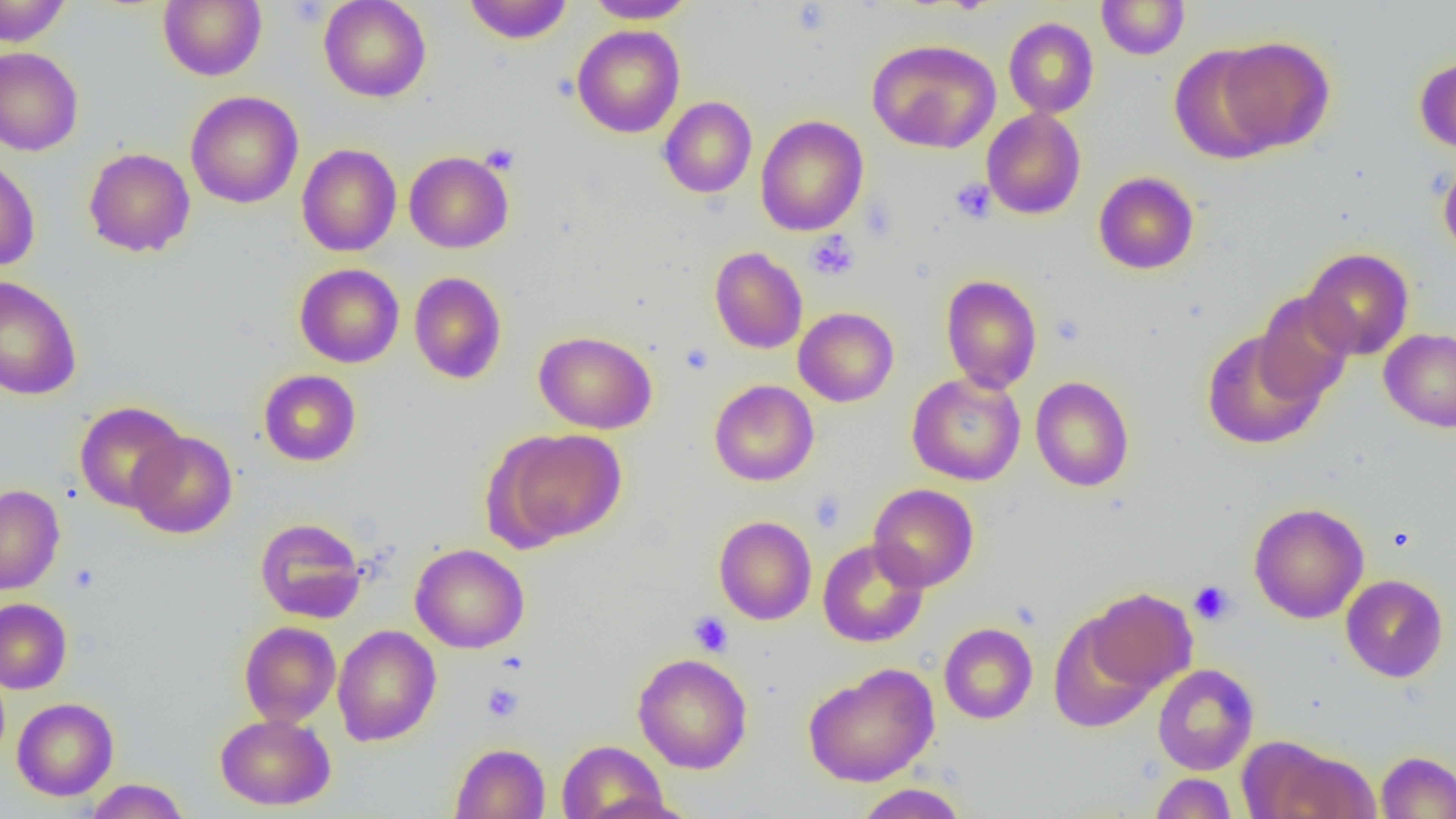

Summary:
  - Coordinate format: approximate bounding boxes as named x1/y1/x2/y2 corners in pixels
  - Uninfected red blood cell locations: (x1=0, y1=0, x2=71, y2=46), (x1=158, y1=0, x2=267, y2=81), (x1=318, y1=0, x2=432, y2=102), (x1=585, y1=0, x2=697, y2=24), (x1=1096, y1=0, x2=1189, y2=60), (x1=463, y1=1, x2=573, y2=44), (x1=1004, y1=17, x2=1099, y2=118), (x1=572, y1=25, x2=685, y2=138), (x1=1215, y1=36, x2=1335, y2=153), (x1=867, y1=38, x2=1001, y2=154), (x1=1169, y1=45, x2=1280, y2=164), (x1=0, y1=48, x2=83, y2=156), (x1=1415, y1=55, x2=1456, y2=154), (x1=186, y1=90, x2=303, y2=209), (x1=659, y1=96, x2=757, y2=198), (x1=981, y1=108, x2=1086, y2=219), (x1=755, y1=115, x2=868, y2=236), (x1=297, y1=143, x2=402, y2=256), (x1=84, y1=147, x2=195, y2=257), (x1=404, y1=151, x2=513, y2=253), (x1=0, y1=157, x2=40, y2=272), (x1=1438, y1=158, x2=1456, y2=262), (x1=1093, y1=171, x2=1199, y2=275), (x1=709, y1=247, x2=808, y2=354), (x1=1301, y1=247, x2=1414, y2=360), (x1=294, y1=263, x2=404, y2=368), (x1=409, y1=272, x2=507, y2=384), (x1=940, y1=274, x2=1042, y2=393), (x1=0, y1=275, x2=82, y2=401), (x1=1254, y1=293, x2=1355, y2=405), (x1=793, y1=307, x2=899, y2=407), (x1=1379, y1=328, x2=1456, y2=432), (x1=1201, y1=329, x2=1325, y2=449), (x1=534, y1=330, x2=657, y2=434), (x1=258, y1=369, x2=361, y2=466), (x1=907, y1=373, x2=1026, y2=486), (x1=1030, y1=376, x2=1135, y2=492), (x1=709, y1=380, x2=819, y2=486), (x1=74, y1=401, x2=189, y2=512), (x1=491, y1=428, x2=626, y2=548), (x1=128, y1=430, x2=238, y2=538), (x1=868, y1=483, x2=979, y2=592), (x1=0, y1=484, x2=65, y2=595), (x1=1248, y1=502, x2=1369, y2=623), (x1=714, y1=516, x2=817, y2=625), (x1=254, y1=517, x2=367, y2=623), (x1=817, y1=539, x2=928, y2=647), (x1=410, y1=543, x2=529, y2=653), (x1=1341, y1=574, x2=1448, y2=682), (x1=1085, y1=587, x2=1197, y2=694), (x1=0, y1=598, x2=71, y2=694), (x1=1048, y1=615, x2=1159, y2=732), (x1=239, y1=621, x2=341, y2=727), (x1=938, y1=622, x2=1038, y2=724), (x1=332, y1=624, x2=441, y2=747), (x1=633, y1=653, x2=753, y2=773), (x1=802, y1=662, x2=940, y2=787), (x1=1152, y1=664, x2=1259, y2=775), (x1=12, y1=697, x2=119, y2=800), (x1=215, y1=713, x2=336, y2=810), (x1=557, y1=739, x2=669, y2=819), (x1=1258, y1=742, x2=1380, y2=818), (x1=450, y1=743, x2=550, y2=819), (x1=1375, y1=751, x2=1456, y2=818), (x1=1150, y1=773, x2=1237, y2=818), (x1=85, y1=778, x2=190, y2=819), (x1=853, y1=783, x2=969, y2=818)
  - Platelet locations: (x1=791, y1=2, x2=832, y2=35), (x1=480, y1=144, x2=519, y2=175), (x1=950, y1=178, x2=996, y2=224), (x1=806, y1=231, x2=860, y2=280), (x1=680, y1=343, x2=714, y2=374), (x1=809, y1=489, x2=847, y2=533), (x1=1188, y1=580, x2=1236, y2=625), (x1=688, y1=611, x2=733, y2=657), (x1=481, y1=683, x2=523, y2=722)
  - Slide-level diagnosis: no evidence of blood parasites
  - Field of view: single
  - Modality: light microscopy
  - Magnification: 1000x
  - Image size: 1456×819 pixels
  - Preparation: thin blood smear